Locate and identify every blood parasite.
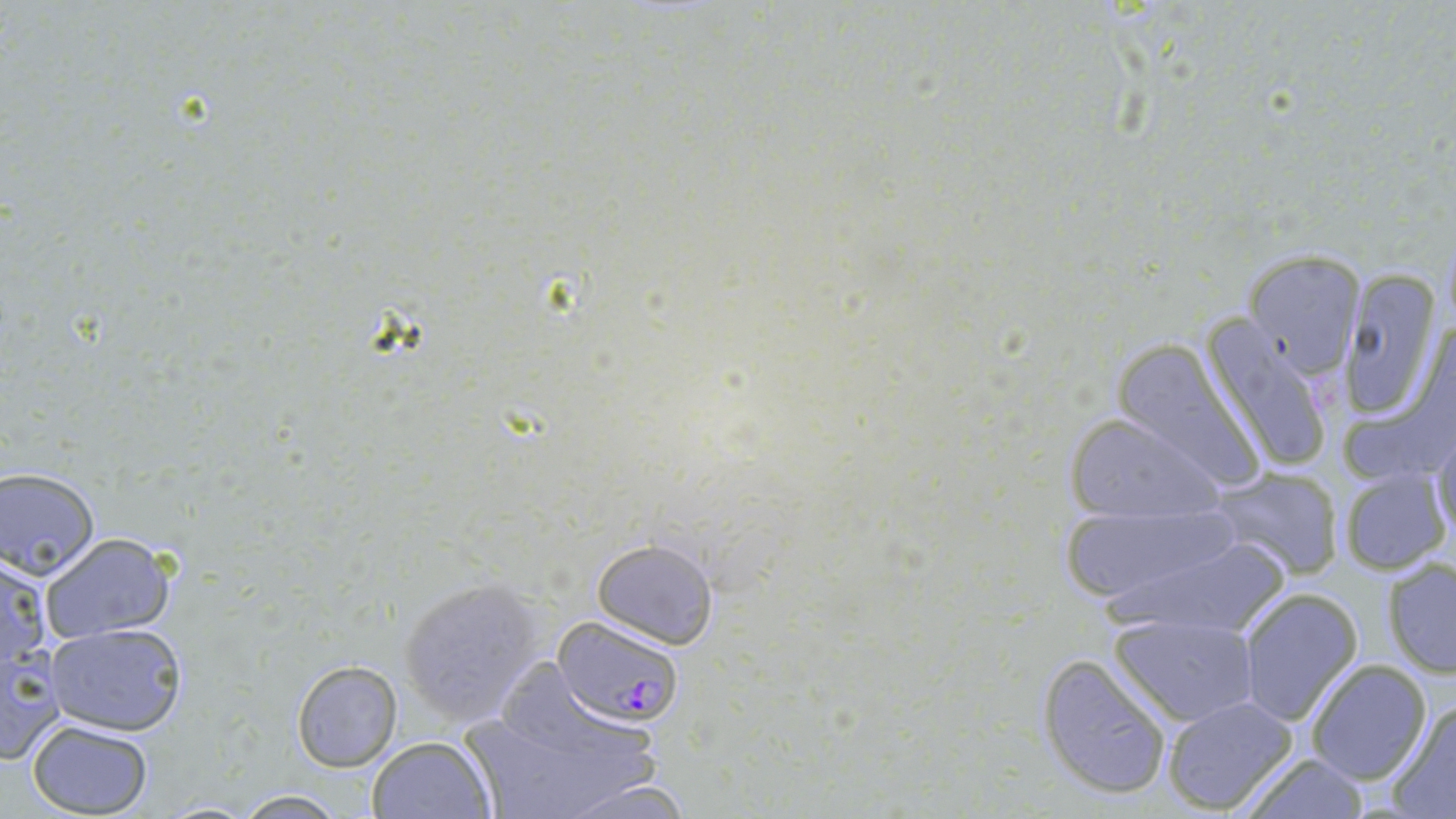

Approximate bounding boxes as [x1, y1, x2, y2] in pixels.
Plasmodium falciparum-infected red blood cells: [555, 616, 687, 727].
No Plasmodium ovale, Plasmodium malariae, Plasmodium vivax, Babesia divergens, or Trypanosoma brucei observed.

Uninfected red blood cell locations: [1238, 250, 1363, 378], [1338, 271, 1444, 419], [1200, 320, 1334, 475], [1104, 340, 1269, 488], [1063, 412, 1222, 527], [1431, 430, 1456, 547], [0, 467, 101, 577], [1206, 467, 1345, 580], [1336, 468, 1450, 574], [1053, 497, 1240, 611], [1104, 528, 1297, 643], [41, 532, 175, 644], [591, 538, 719, 649], [0, 555, 50, 672], [1382, 558, 1456, 678], [397, 575, 550, 727], [1237, 587, 1362, 725], [1109, 612, 1258, 725], [45, 622, 188, 738], [0, 643, 65, 766], [1037, 653, 1173, 801], [291, 659, 404, 772], [1306, 660, 1432, 785], [1161, 694, 1300, 817], [1383, 699, 1456, 818], [459, 700, 661, 819], [27, 719, 154, 817], [365, 735, 495, 819], [1234, 752, 1372, 818], [558, 776, 700, 817], [230, 790, 351, 818]. Slide-level diagnosis: Plasmodium falciparum. Image is 1456×819 pixels. Single field of view. May-Grünwald-Giemsa stain. Thin blood film. Light microscopy. 1000x magnification.